Point out each leukocyte.
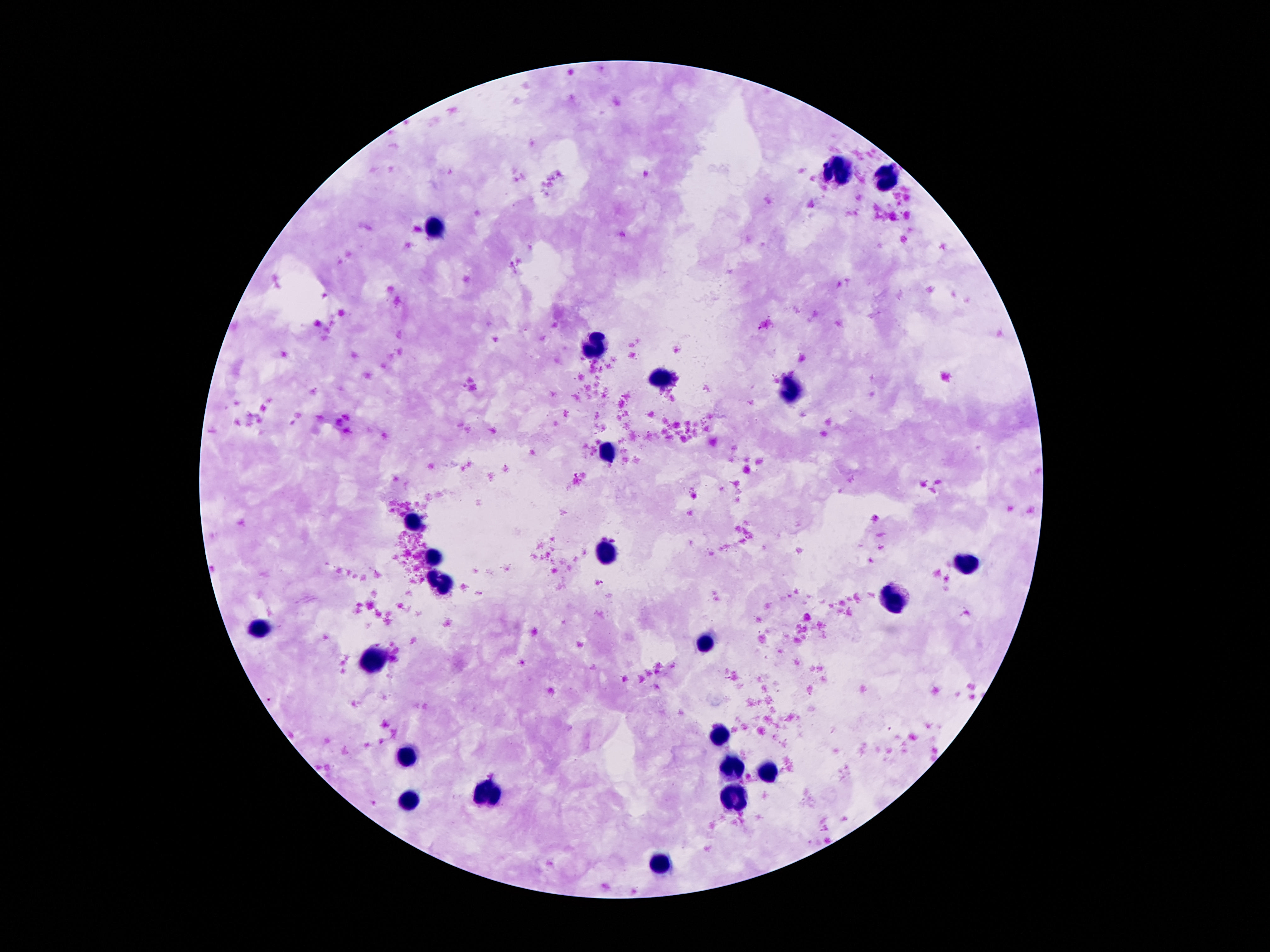
Approximate centers as [x, y] in pixels.
Leukocytes: [837, 171], [887, 179], [435, 227], [592, 345], [665, 380], [784, 393], [607, 453], [413, 520], [605, 548], [435, 556], [969, 563], [441, 583], [895, 602], [260, 628], [706, 645], [377, 660], [717, 735], [405, 760], [732, 768], [766, 773], [491, 792], [730, 796], [409, 800], [663, 862].

100x magnification. Thick blood smear. Giemsa stain. Image is 1270×952 pixels. Patient malaria status: negative. One field from this slide. Smartphone photograph taken through the microscope eyepiece.